Locate every blood parasite and identify its species.
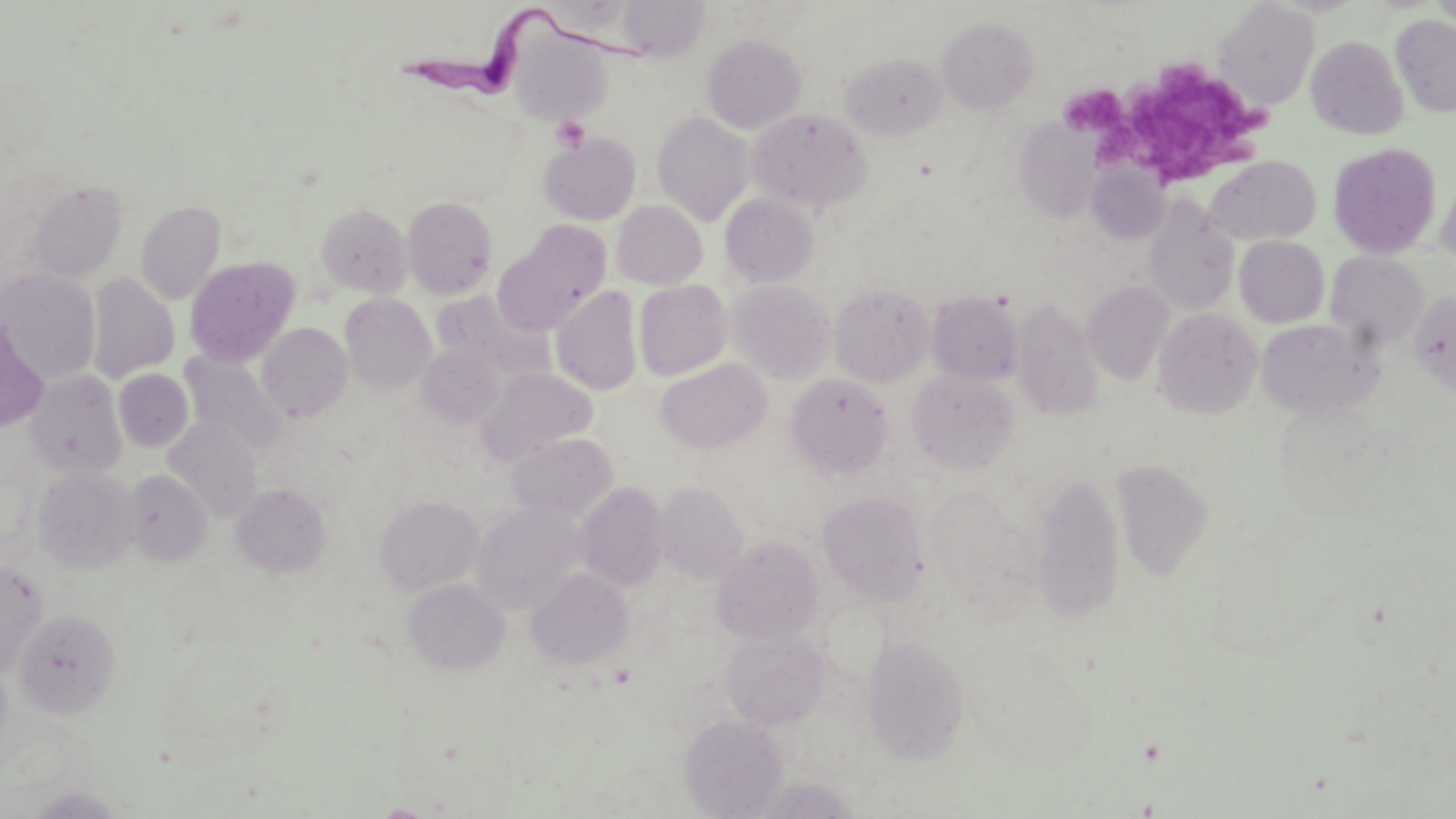

Approximate bounding boxes as [x1, y1, x2, y2] in pixels.
Trypanosoma brucei: [399, 7, 669, 116].
No Plasmodium falciparum, Plasmodium ovale, Plasmodium malariae, Plasmodium vivax, or Babesia divergens observed.

{
  "slide_level_diagnosis": "Trypanosoma brucei",
  "magnification": "1000x",
  "field_of_view": "single",
  "preparation": "thin blood smear",
  "uninfected_red_blood_cell_locations": "approximate bounding boxes as [x1, y1, x2, y2] in pixels: [1428, 0, 1456, 27], [1213, 2, 1319, 110], [1391, 14, 1456, 117], [937, 17, 1039, 114], [508, 25, 614, 126], [702, 34, 806, 133], [1305, 36, 1409, 140], [841, 52, 946, 139], [748, 108, 873, 212], [652, 111, 754, 226], [1015, 120, 1101, 221], [539, 132, 641, 225], [1327, 143, 1442, 258], [1205, 155, 1321, 245], [1088, 160, 1169, 243], [1436, 170, 1456, 267], [26, 180, 127, 283], [720, 193, 819, 287], [402, 196, 498, 299], [1142, 197, 1239, 315], [135, 201, 226, 304], [612, 201, 707, 289], [315, 203, 412, 298], [496, 221, 613, 332], [1235, 236, 1330, 327], [1326, 251, 1429, 352], [184, 257, 300, 365], [0, 270, 100, 383], [86, 272, 180, 383], [634, 280, 732, 380], [728, 280, 836, 383], [1084, 281, 1174, 385], [829, 282, 935, 386], [551, 286, 643, 395], [432, 291, 555, 386], [927, 291, 1023, 384], [1409, 291, 1456, 394], [340, 293, 436, 393], [1012, 298, 1105, 422], [1152, 308, 1263, 418], [1256, 318, 1382, 419], [257, 323, 352, 422], [418, 343, 507, 426], [181, 352, 290, 455], [655, 359, 772, 454], [476, 367, 597, 466], [113, 369, 194, 451], [25, 370, 127, 477], [907, 370, 1019, 474], [786, 374, 893, 477], [164, 418, 261, 519], [508, 433, 618, 522], [1113, 459, 1213, 580], [33, 466, 139, 575], [124, 469, 213, 567], [1033, 471, 1125, 620], [576, 482, 669, 590], [656, 482, 748, 584], [231, 483, 331, 578], [926, 485, 1035, 605], [818, 491, 928, 603], [375, 495, 483, 595], [472, 502, 586, 612], [712, 536, 824, 645], [0, 560, 48, 676], [526, 568, 634, 669], [403, 578, 511, 674], [13, 608, 120, 719], [721, 629, 830, 730], [861, 635, 970, 763], [680, 713, 788, 818]",
  "platelet_locations": "approximate bounding boxes as [x1, y1, x2, y2] in pixels: [1107, 64, 1280, 180], [1064, 86, 1126, 136], [550, 115, 590, 150]",
  "modality": "optical microscopy",
  "image_size": "1456×819 pixels",
  "stain": "May-Grünwald-Giemsa"
}